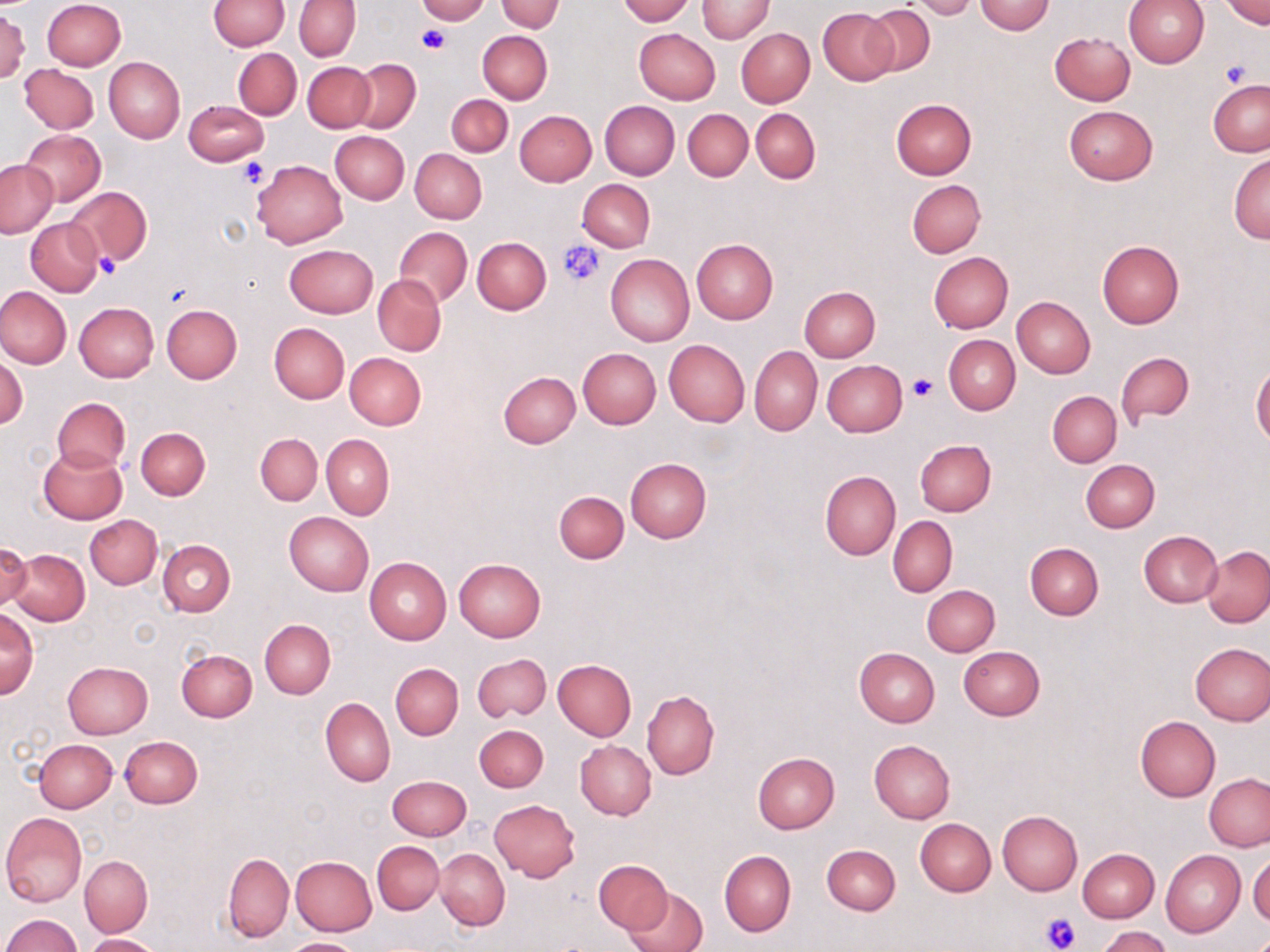 Approximate bounding boxes as named x1/y1/x2/y2 corners in pixels. Platelet locations: (x1=417, y1=26, x2=449, y2=55), (x1=1220, y1=61, x2=1250, y2=88), (x1=237, y1=157, x2=268, y2=187), (x1=557, y1=239, x2=606, y2=287), (x1=95, y1=254, x2=119, y2=280), (x1=907, y1=374, x2=938, y2=402), (x1=1040, y1=912, x2=1081, y2=952). Uninfected red blood cell locations: (x1=41, y1=0, x2=124, y2=71), (x1=416, y1=0, x2=489, y2=24), (x1=497, y1=0, x2=563, y2=32), (x1=617, y1=0, x2=694, y2=25), (x1=697, y1=0, x2=774, y2=42), (x1=1123, y1=0, x2=1210, y2=67), (x1=1223, y1=0, x2=1269, y2=28), (x1=208, y1=1, x2=289, y2=50), (x1=295, y1=1, x2=361, y2=60), (x1=910, y1=1, x2=978, y2=20), (x1=975, y1=1, x2=1055, y2=35), (x1=864, y1=5, x2=935, y2=75), (x1=819, y1=7, x2=898, y2=84), (x1=0, y1=9, x2=30, y2=83), (x1=634, y1=28, x2=720, y2=104), (x1=736, y1=28, x2=814, y2=107), (x1=478, y1=31, x2=552, y2=104), (x1=1050, y1=31, x2=1135, y2=105), (x1=232, y1=48, x2=302, y2=120), (x1=205, y1=55, x2=294, y2=156), (x1=105, y1=56, x2=185, y2=144), (x1=350, y1=59, x2=421, y2=133), (x1=302, y1=61, x2=374, y2=132), (x1=20, y1=64, x2=98, y2=134), (x1=1208, y1=80, x2=1270, y2=156), (x1=446, y1=94, x2=513, y2=156), (x1=890, y1=99, x2=976, y2=179), (x1=183, y1=100, x2=268, y2=166), (x1=600, y1=100, x2=679, y2=179), (x1=1064, y1=105, x2=1157, y2=184), (x1=683, y1=109, x2=753, y2=181), (x1=751, y1=109, x2=820, y2=184), (x1=513, y1=110, x2=596, y2=186), (x1=21, y1=129, x2=106, y2=206), (x1=330, y1=130, x2=409, y2=203), (x1=409, y1=149, x2=486, y2=223), (x1=1228, y1=152, x2=1269, y2=243), (x1=0, y1=159, x2=58, y2=239), (x1=251, y1=160, x2=348, y2=248), (x1=577, y1=179, x2=655, y2=252), (x1=908, y1=179, x2=985, y2=257), (x1=65, y1=186, x2=151, y2=268), (x1=26, y1=218, x2=104, y2=297), (x1=396, y1=227, x2=472, y2=306), (x1=473, y1=237, x2=550, y2=314), (x1=691, y1=238, x2=778, y2=324), (x1=1097, y1=240, x2=1184, y2=327), (x1=284, y1=244, x2=377, y2=317), (x1=929, y1=252, x2=1013, y2=333), (x1=606, y1=254, x2=694, y2=345), (x1=373, y1=275, x2=446, y2=355), (x1=363, y1=276, x2=438, y2=428), (x1=0, y1=286, x2=72, y2=369), (x1=799, y1=286, x2=880, y2=362), (x1=1012, y1=297, x2=1095, y2=378), (x1=73, y1=302, x2=158, y2=382), (x1=162, y1=304, x2=242, y2=383), (x1=269, y1=322, x2=349, y2=404), (x1=943, y1=336, x2=1019, y2=414), (x1=663, y1=339, x2=749, y2=428), (x1=750, y1=345, x2=822, y2=437), (x1=577, y1=347, x2=661, y2=428), (x1=1115, y1=351, x2=1195, y2=427), (x1=344, y1=352, x2=426, y2=430), (x1=0, y1=355, x2=28, y2=429), (x1=822, y1=360, x2=906, y2=436), (x1=1251, y1=363, x2=1270, y2=447), (x1=499, y1=371, x2=581, y2=448), (x1=1047, y1=391, x2=1121, y2=467), (x1=52, y1=398, x2=130, y2=472), (x1=136, y1=428, x2=209, y2=500), (x1=255, y1=433, x2=322, y2=505), (x1=322, y1=434, x2=394, y2=521), (x1=915, y1=439, x2=995, y2=517), (x1=38, y1=447, x2=127, y2=524), (x1=625, y1=459, x2=712, y2=542), (x1=1081, y1=459, x2=1159, y2=532), (x1=820, y1=469, x2=900, y2=560), (x1=554, y1=491, x2=629, y2=563), (x1=284, y1=512, x2=374, y2=595), (x1=86, y1=515, x2=162, y2=588), (x1=888, y1=516, x2=956, y2=596), (x1=1138, y1=530, x2=1222, y2=606), (x1=157, y1=539, x2=235, y2=616), (x1=0, y1=542, x2=32, y2=612), (x1=1025, y1=543, x2=1103, y2=620), (x1=1202, y1=546, x2=1270, y2=627), (x1=12, y1=547, x2=90, y2=626), (x1=365, y1=557, x2=452, y2=644), (x1=454, y1=558, x2=546, y2=641), (x1=922, y1=584, x2=1000, y2=657), (x1=0, y1=608, x2=39, y2=698), (x1=260, y1=620, x2=334, y2=698), (x1=1190, y1=642, x2=1270, y2=725), (x1=853, y1=646, x2=940, y2=726), (x1=958, y1=646, x2=1046, y2=720), (x1=176, y1=648, x2=257, y2=723), (x1=473, y1=653, x2=551, y2=723), (x1=552, y1=659, x2=637, y2=741), (x1=63, y1=661, x2=153, y2=738), (x1=391, y1=663, x2=463, y2=739), (x1=642, y1=690, x2=719, y2=780), (x1=321, y1=697, x2=395, y2=787), (x1=1136, y1=716, x2=1220, y2=801), (x1=474, y1=725, x2=548, y2=792), (x1=120, y1=736, x2=203, y2=808), (x1=35, y1=739, x2=117, y2=812), (x1=868, y1=739, x2=955, y2=824), (x1=575, y1=742, x2=655, y2=820), (x1=753, y1=751, x2=839, y2=832), (x1=387, y1=774, x2=472, y2=840), (x1=1204, y1=775, x2=1270, y2=851), (x1=490, y1=799, x2=581, y2=881), (x1=997, y1=810, x2=1083, y2=895), (x1=1, y1=812, x2=87, y2=908), (x1=916, y1=818, x2=996, y2=896), (x1=372, y1=842, x2=443, y2=914), (x1=821, y1=844, x2=901, y2=915), (x1=1077, y1=847, x2=1159, y2=922), (x1=435, y1=848, x2=510, y2=930), (x1=719, y1=849, x2=795, y2=937), (x1=1161, y1=849, x2=1246, y2=937), (x1=223, y1=852, x2=294, y2=942), (x1=1249, y1=854, x2=1270, y2=924), (x1=80, y1=855, x2=152, y2=937), (x1=290, y1=856, x2=378, y2=936), (x1=594, y1=859, x2=672, y2=934), (x1=624, y1=885, x2=707, y2=952), (x1=1, y1=914, x2=82, y2=952), (x1=1099, y1=926, x2=1170, y2=952), (x1=85, y1=934, x2=160, y2=952), (x1=282, y1=937, x2=362, y2=952). Slide-level diagnosis: negative for blood parasites. Image is 1270×952 pixels. Light microscopy. One field of a larger specimen. 1000x magnification. May-Grünwald-Giemsa stain. Thin blood smear.